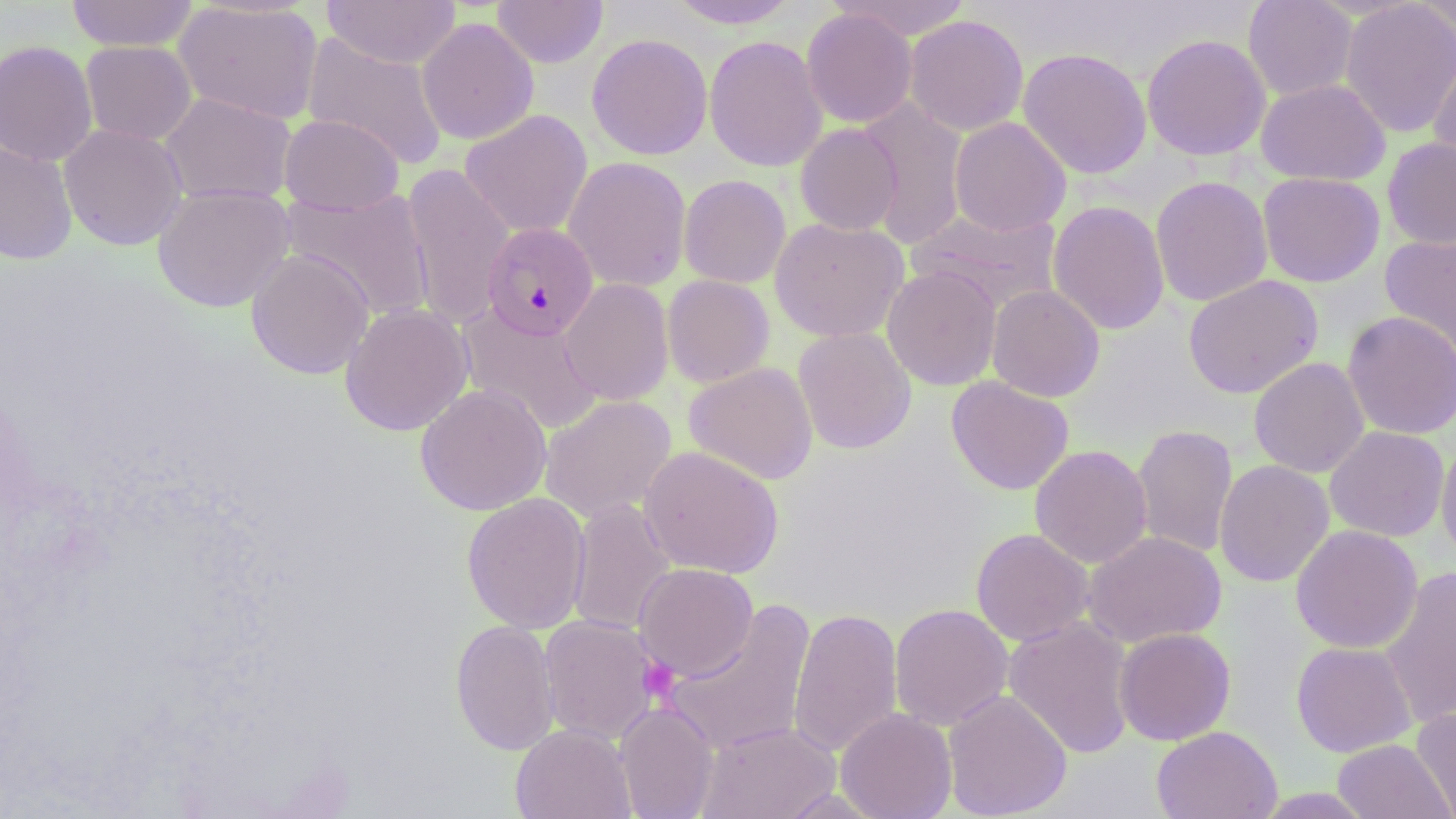

slide_level_diagnosis: Plasmodium falciparum
magnification: 1000x
field_of_view: one of a larger specimen
stain: May-Grünwald-Giemsa
plasmodium_falciparum_infected_red_blood_cell_locations: 'approximate bounding boxes as (x1,y1)-(x2,y2) corner pairs in pixels: (481,222)-(599,341)'
uninfected_red_blood_cell_locations: 'approximate bounding boxes as (x1,y1)-(x2,y2) corner pairs in pixels: (65,0)-(199,52), (173,0)-(324,125), (322,0)-(461,69), (492,0)-(608,68), (665,0)-(801,29), (830,0)-(974,40), (1243,0)-(1358,101), (1340,0)-(1456,138), (1416,0)-(1456,41), (801,8)-(918,128), (904,15)-(1029,136), (416,17)-(539,145), (303,33)-(449,169), (586,33)-(713,160), (1141,34)-(1271,161), (704,35)-(828,172), (0,40)-(99,167), (81,40)-(196,145), (1018,47)-(1153,179), (1427,47)-(1456,172), (1256,78)-(1391,185), (159,91)-(297,206), (857,98)-(969,250), (460,110)-(593,239), (279,114)-(404,215), (949,117)-(1071,236), (58,123)-(188,251), (795,123)-(903,236), (1382,137)-(1456,250), (0,140)-(78,266), (563,156)-(691,292), (401,163)-(516,329), (1257,172)-(1385,287), (679,174)-(791,288), (1150,175)-(1273,307), (152,184)-(295,312), (281,186)-(435,321), (1047,200)-(1170,335), (907,208)-(1063,312), (770,217)-(909,343), (1379,232)-(1456,358), (246,249)-(375,379), (882,265)-(1001,390), (661,274)-(775,388), (1183,274)-(1324,398), (559,278)-(674,405), (986,285)-(1105,402), (340,303)-(474,436), (456,303)-(604,436), (1341,310)-(1456,440), (793,326)-(917,455), (1248,357)-(1370,478), (684,362)-(818,485), (946,376)-(1074,495), (415,383)-(552,515), (539,395)-(677,523), (1132,424)-(1238,559), (1324,425)-(1450,542), (1436,437)-(1456,566), (639,445)-(784,579), (1029,445)-(1152,568), (1214,459)-(1335,587), (461,492)-(591,634), (566,499)-(677,637), (1290,524)-(1423,654), (970,528)-(1093,646), (1083,531)-(1227,648), (634,563)-(758,681), (1379,567)-(1456,728), (663,601)-(816,755), (889,603)-(1013,730), (788,607)-(904,758), (538,615)-(662,745), (1003,616)-(1137,759), (450,619)-(560,755), (1114,627)-(1236,745), (1291,641)-(1417,757), (943,689)-(1072,819), (615,702)-(719,819), (1411,706)-(1456,819), (835,707)-(957,819), (696,721)-(840,818), (510,723)-(636,819), (1151,725)-(1283,819), (1332,739)-(1454,819)'
preparation: thin blood film
platelet_locations: 'approximate bounding boxes as (x1,y1)-(x2,y2) corner pairs in pixels: (638,657)-(679,702)'
image_size: 1456×819 pixels
modality: optical microscopy